Identify the parasite.
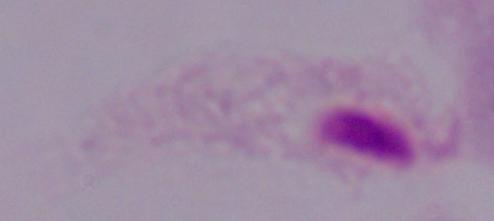

A trichomonad.

Photomicrograph. Captured at 1000x magnification.